Report the malaria status of this cell.
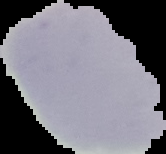
Uninfected.

Summary:
  - Image type: segmented cell region on a black background
  - Preparation: thin blood film
  - Image size: 166×154 pixels